Name the parasite shown.
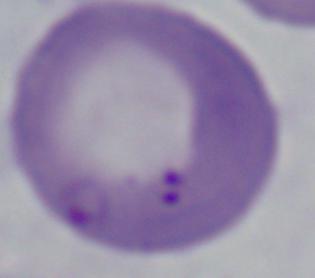
This is Babesia.

Micrograph. Captured at 1000x magnification.